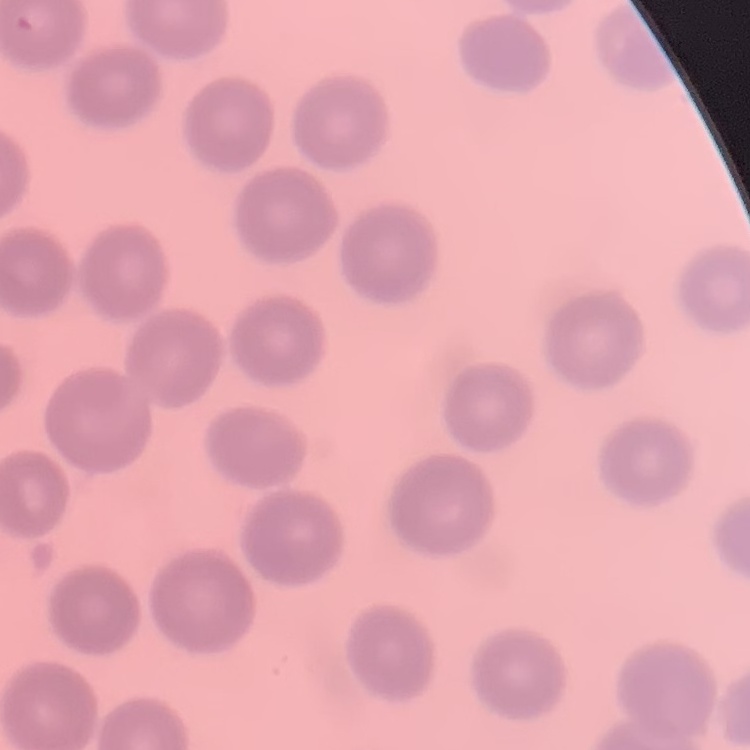
red_blood_cell_morphology: no rouleaux formation
preparation: thin blood smear
image_type: square crop of a larger photomicrograph
stain: Field's or Giemsa